State the preparation type.
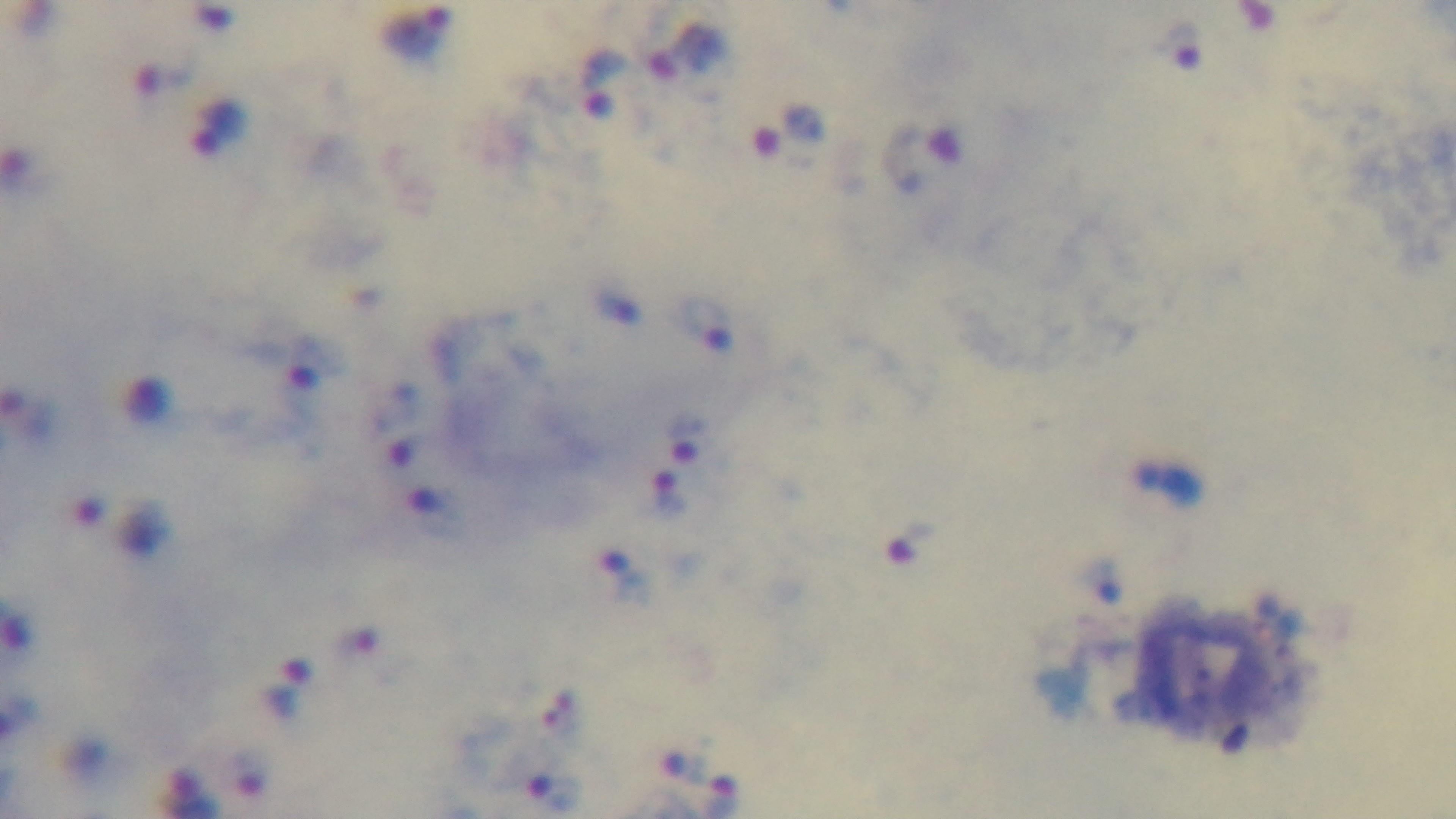
It is a thick blood film.

Giemsa stain. Captured with a mounted 4K digital camera. 100x oil-immersion objective. Single field of view. Photomicrograph. Malaria status: infected.